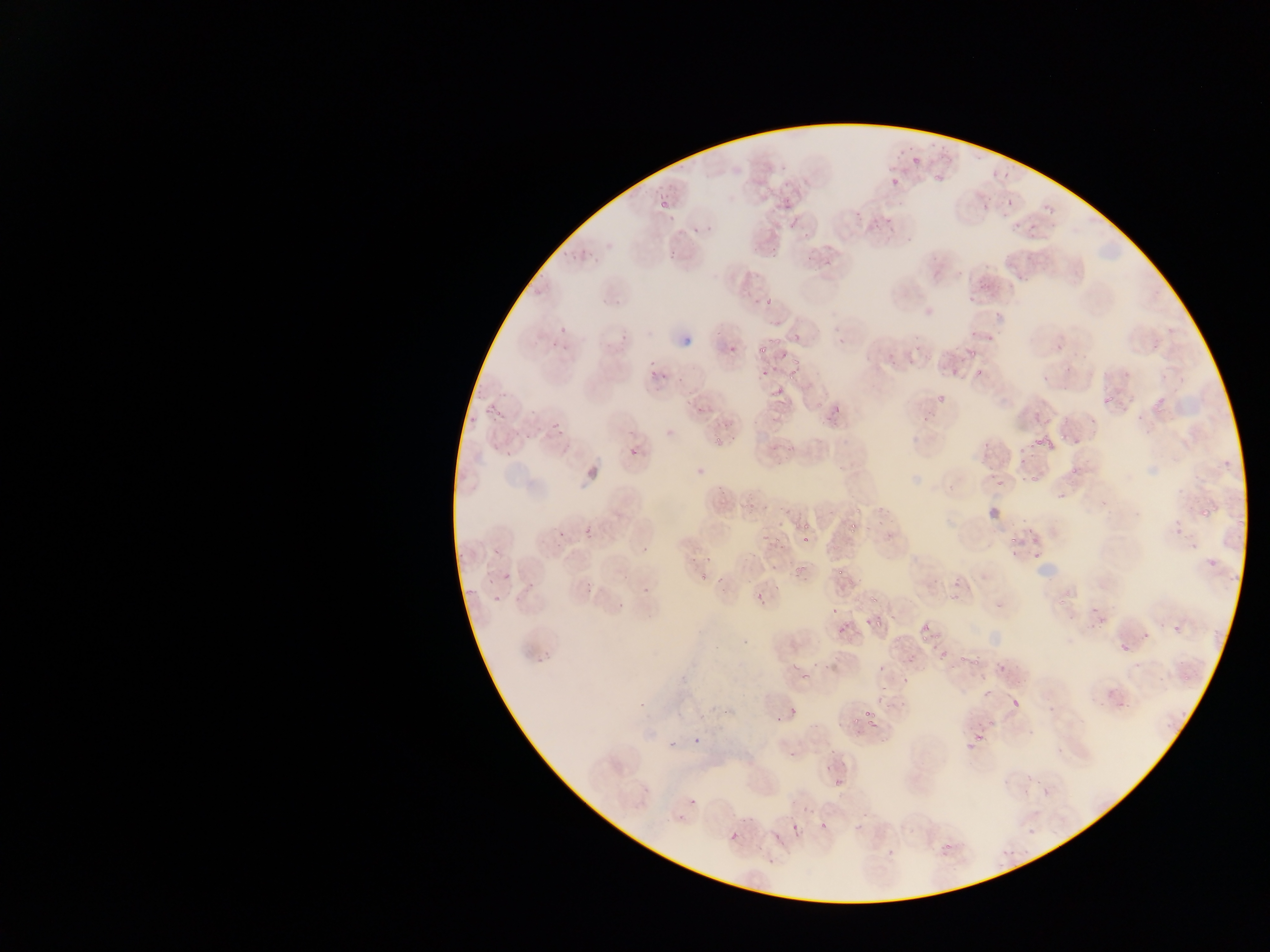 Approximate bounding boxes as {left, top, right, bottom} in pixels. Malaria parasite locations (subset; some below the resolvable size): {937, 141, 950, 152}, {895, 146, 910, 158}, {907, 157, 927, 168}, {1000, 159, 1022, 183}, {777, 165, 788, 175}, {930, 168, 948, 183}, {780, 193, 792, 205}, {653, 194, 670, 211}, {1006, 196, 1019, 206}, {980, 198, 992, 210}, {1041, 199, 1055, 214}, {1000, 206, 1008, 216}, {854, 211, 861, 223}, {665, 215, 676, 222}, {885, 216, 899, 235}, {865, 217, 878, 228}, {1029, 221, 1044, 237}, {704, 223, 715, 233}, {1011, 224, 1021, 232}, {692, 227, 704, 238}, {800, 229, 810, 238}, {771, 246, 779, 255}, {666, 247, 684, 260}, {571, 248, 593, 267}, {820, 251, 839, 266}, {1015, 273, 1027, 282}, {992, 279, 1006, 291}, {965, 292, 978, 303}, {615, 293, 630, 307}, {762, 296, 776, 311}, {993, 307, 1006, 318}, {718, 325, 759, 364}, {554, 328, 586, 356}, {983, 331, 995, 341}, {834, 333, 847, 348}, {911, 333, 918, 342}, {783, 334, 802, 343}, {1055, 342, 1063, 350}, {754, 343, 774, 355}, {969, 348, 982, 359}, {790, 350, 801, 367}, {905, 353, 919, 368}, {889, 360, 898, 372}, {645, 366, 658, 376}, {1065, 366, 1072, 374}, {662, 367, 671, 384}, {786, 367, 803, 378}, {973, 368, 987, 379}, {759, 369, 771, 380}, {473, 381, 488, 402}, {494, 389, 507, 399}, {772, 389, 783, 399}, {937, 393, 950, 405}, {682, 395, 693, 405}, {1103, 399, 1113, 405}, {489, 400, 508, 420}, {1150, 403, 1162, 410}, {528, 405, 540, 416}, {693, 406, 703, 414}, {821, 408, 842, 426}, {919, 411, 936, 429}, {463, 413, 476, 427}, {720, 413, 741, 431}, {542, 415, 561, 436}, {1089, 418, 1098, 427}, {1035, 430, 1055, 446}, {711, 436, 723, 446}, {1072, 438, 1081, 446}, {502, 441, 524, 463}, {627, 444, 638, 454}, {980, 449, 994, 461}, {1020, 457, 1027, 468}, {688, 463, 705, 480}, {1068, 463, 1088, 475}, {987, 472, 995, 480}, {1029, 473, 1039, 481}, {996, 475, 1011, 487}, {1055, 487, 1075, 502}, {1197, 506, 1212, 516}, {1170, 515, 1188, 528}, {800, 520, 818, 536}, {583, 524, 594, 535}, {848, 524, 862, 538}, {557, 529, 568, 539}, {760, 532, 772, 543}, {800, 532, 813, 547}, {772, 534, 782, 542}, {1005, 536, 1020, 546}, {1188, 538, 1201, 550}, {642, 542, 651, 554}, {1031, 545, 1048, 560}, {1010, 549, 1019, 558}, {1204, 551, 1216, 568}, {476, 552, 499, 584}, {700, 558, 712, 566}, {793, 562, 807, 574}, {835, 565, 848, 578}, {498, 567, 526, 612}, {699, 567, 713, 584}, {713, 568, 728, 589}, {952, 570, 963, 585}, {1223, 571, 1241, 582}, {582, 578, 593, 597}, {636, 580, 658, 597}, {528, 583, 538, 590}, {758, 587, 779, 602}, {867, 591, 887, 603}, {949, 595, 960, 601}, {1058, 595, 1070, 608}, {612, 599, 623, 622}, {828, 603, 841, 616}, {1087, 606, 1104, 620}, {873, 615, 889, 632}, {863, 616, 874, 631}, {1088, 619, 1105, 631}, {917, 620, 938, 644}, {838, 623, 852, 636}, {1172, 625, 1182, 635}, {1138, 628, 1151, 641}, {1113, 638, 1127, 657}, {956, 650, 969, 661}, {970, 652, 988, 666}, {874, 664, 886, 672}, {797, 666, 820, 686}, {1181, 666, 1194, 684}, {899, 675, 910, 684}, {872, 685, 890, 698}, {982, 685, 997, 697}, {1115, 695, 1127, 707}, {1011, 698, 1019, 706}, {1179, 703, 1190, 717}, {1165, 705, 1181, 728}, {790, 707, 800, 716}, {859, 708, 884, 729}, {774, 714, 786, 728}, {985, 721, 1000, 731}, {691, 730, 705, 747}, {972, 730, 991, 754}, {662, 734, 681, 757}, {828, 745, 838, 755}, {786, 746, 800, 759}, {1024, 762, 1040, 784}, {813, 765, 834, 773}, {831, 775, 844, 787}, {688, 798, 696, 807}, {800, 802, 812, 812}, {677, 814, 685, 824}, {818, 815, 832, 830}, {793, 822, 801, 834}, {853, 823, 864, 832}, {1026, 823, 1039, 835}, {729, 831, 739, 841}, {942, 840, 954, 849}, {884, 847, 902, 857} | approximate {x, y} pixel centers of objects too small to bound: {894, 180}, {971, 336}. Photographed through a microscope with a mobile-phone camera. Image is 1270×952 pixels. Collected in Ghana. Thin blood smear. One field of view.